Give the position of every Plasmodium parasite visible.
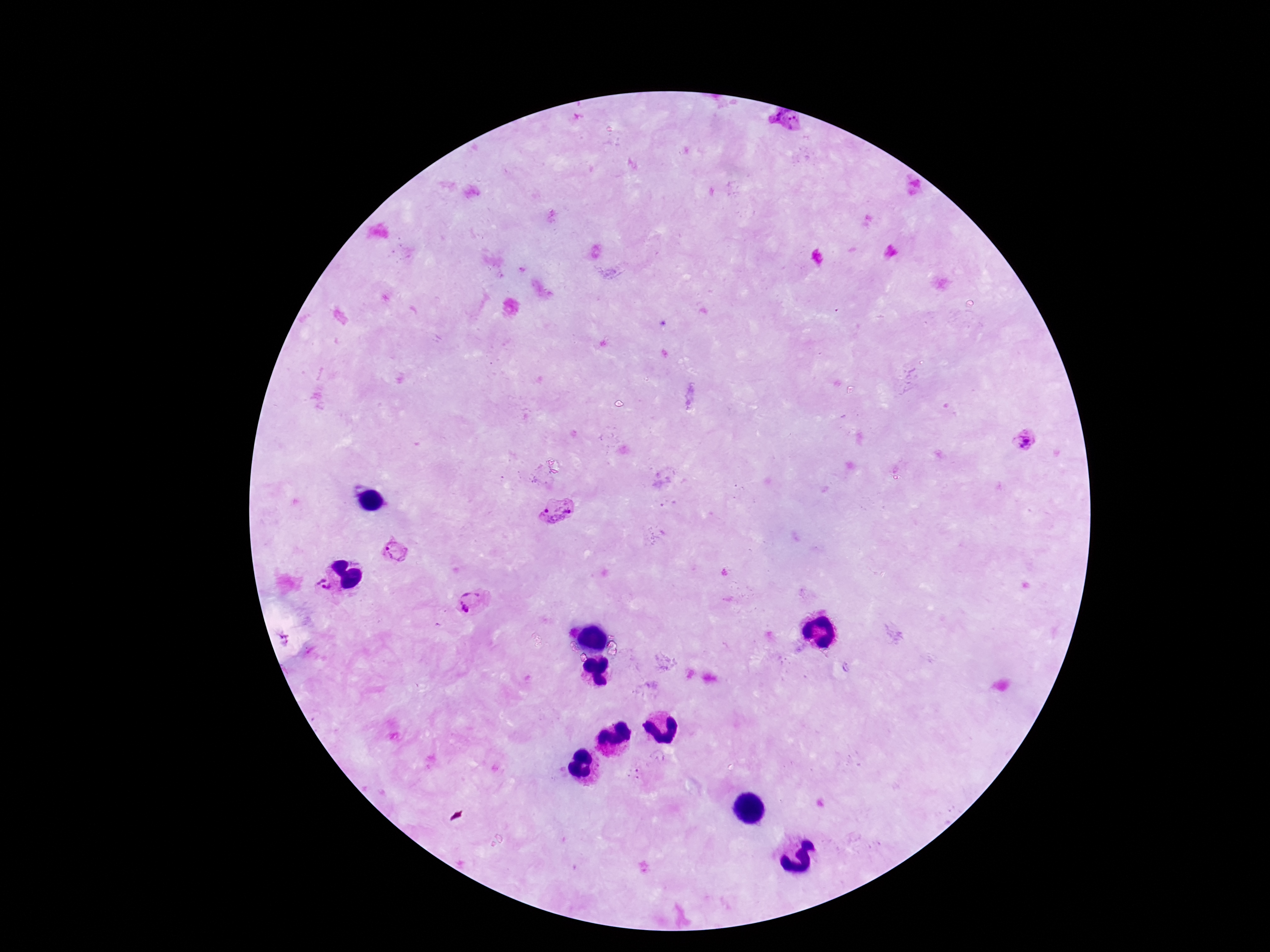

Approximate centers as (x, y) in pixels.
Plasmodium parasites: (785, 123), (1024, 439), (554, 511), (394, 551), (321, 585), (470, 602), (280, 639).

Summary:
  - Preparation: thick peripheral-blood smear
  - Capture: smartphone camera through the microscope eyepiece
  - Patient malaria status: infected
  - Magnification: 100x
  - Image size: 1270×952 pixels
  - Field of view: single
  - Stain: Giemsa